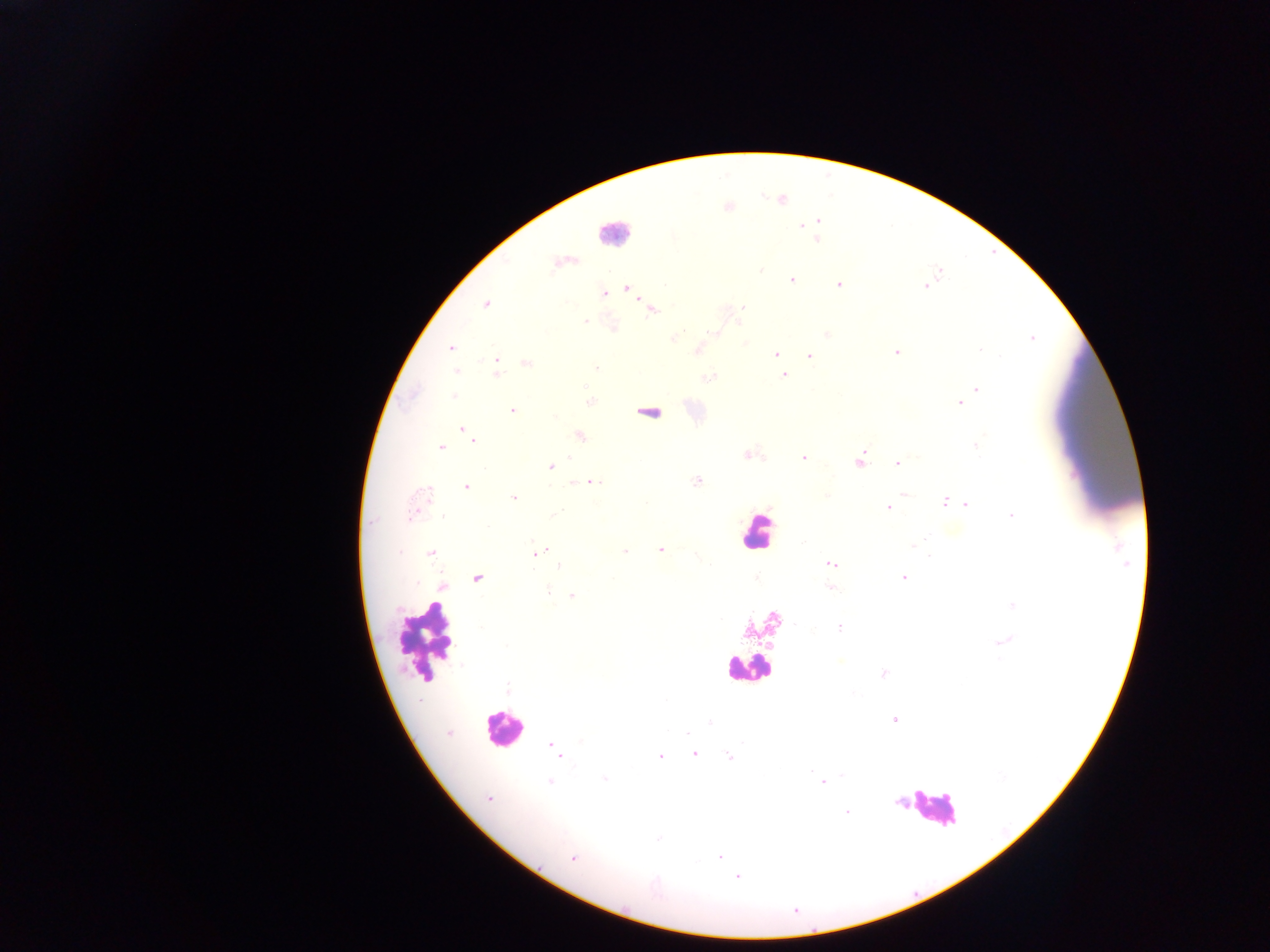
Approximate centers as [x, y] in pixels. Plasmodium parasite locations: [728, 209], [818, 220], [802, 225], [818, 238], [790, 280], [838, 284], [923, 287], [626, 289], [606, 293], [486, 304], [742, 307], [651, 311], [741, 319], [586, 321], [711, 333], [673, 338], [450, 348], [696, 349], [980, 350], [896, 352], [775, 354], [810, 354], [496, 360], [526, 364], [596, 368], [455, 372], [784, 375], [497, 376], [585, 386], [978, 389], [454, 395], [960, 404], [512, 409], [465, 429], [579, 435], [472, 438], [975, 447], [441, 448], [748, 455], [803, 456], [860, 462], [897, 464], [550, 467], [697, 481], [594, 483], [467, 486], [514, 499], [944, 501], [965, 503], [889, 507], [1010, 514], [914, 544], [660, 549], [623, 550], [540, 551], [431, 553], [833, 565], [903, 577], [478, 578], [441, 584], [830, 587], [549, 588], [572, 596], [839, 627], [506, 647], [840, 662], [883, 673], [895, 721], [448, 734], [552, 743], [558, 752], [694, 753], [729, 755], [660, 756], [606, 780], [550, 782], [822, 782], [489, 798], [847, 812], [658, 838], [721, 856], [574, 860], [739, 877]. Leukocyte locations: [613, 235], [649, 407], [755, 527], [426, 641], [750, 667], [504, 727], [936, 808]. Collected in Ghana. Image is 1270×952 pixels. One field of view. Thick blood smear. Photographed through a microscope with a mobile-phone camera.